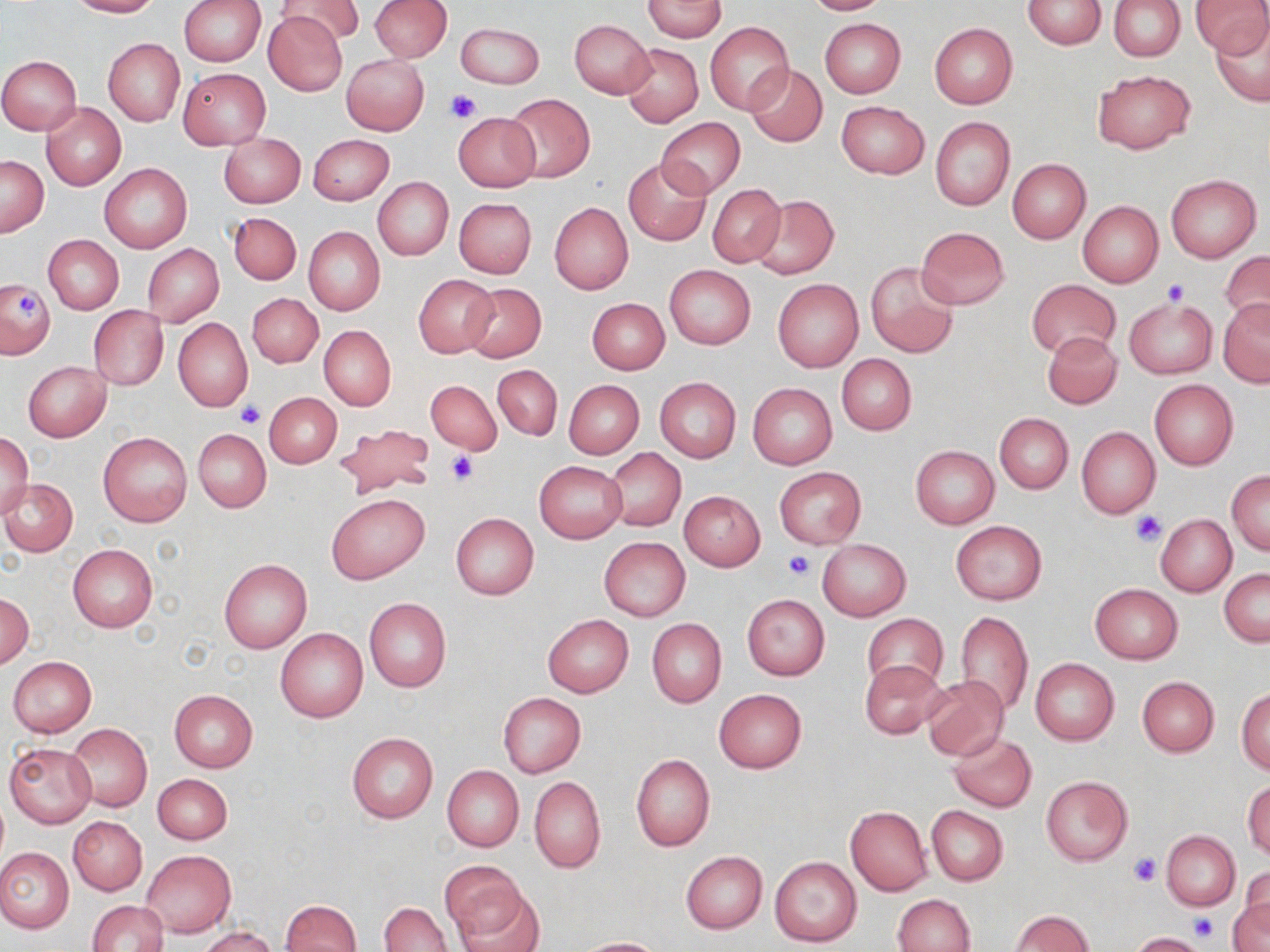

slide_level_diagnosis: negative for blood parasites
magnification: 1000x
stain: May-Grünwald-Giemsa
field_of_view: single
platelet_locations: 'approximate bounding boxes as (x1,y1)-(x2,y2) corner pairs in pixels: (445,89)-(480,123), (1162,279)-(1191,305), (16,291)-(44,315), (237,401)-(265,429), (444,450)-(478,485), (1131,510)-(1167,545), (783,551)-(813,581), (1128,851)-(1160,886), (1188,913)-(1220,943)'
modality: light microscopy
preparation: thin blood film
image_size: 1270×952 pixels
uninfected_red_blood_cell_locations: 'approximate bounding boxes as (x1,y1)-(x2,y2) corner pairs in pixels: (68,0)-(160,17), (178,0)-(264,66), (277,0)-(365,45), (370,0)-(451,62), (642,0)-(727,40), (802,0)-(890,15), (1022,0)-(1107,48), (1109,0)-(1185,61), (1192,1)-(1269,55), (262,10)-(348,97), (1209,15)-(1270,107), (819,18)-(906,98), (569,19)-(654,98), (826,19)-(910,179), (455,22)-(545,89), (705,22)-(793,114), (929,23)-(1017,107), (103,38)-(184,126), (620,43)-(703,128), (342,54)-(428,135), (0,56)-(81,135), (745,63)-(828,147), (179,69)-(269,149), (1092,70)-(1195,154), (504,93)-(595,183), (836,101)-(929,179), (41,103)-(125,190), (452,112)-(541,192), (929,116)-(1014,211), (657,119)-(746,197), (218,133)-(305,208), (308,134)-(393,205), (1,156)-(47,236), (623,158)-(712,247), (1007,159)-(1091,243), (100,163)-(191,252), (1165,174)-(1261,262), (372,178)-(453,261), (707,183)-(786,267), (749,195)-(838,280), (454,197)-(537,279), (1077,200)-(1163,286), (549,202)-(633,295), (228,213)-(301,284), (304,227)-(385,317), (916,227)-(1010,309), (44,235)-(123,314), (142,245)-(224,326), (1219,249)-(1270,330), (865,261)-(960,358), (664,265)-(755,349), (413,275)-(499,357), (0,278)-(55,359), (773,279)-(863,371), (1026,279)-(1121,358), (462,282)-(546,361), (247,294)-(323,368), (587,298)-(669,375), (1124,298)-(1217,379), (1218,298)-(1270,388), (90,306)-(168,390), (173,318)-(253,413), (319,325)-(395,410), (1042,332)-(1121,409), (837,354)-(917,436), (23,361)-(110,441), (493,365)-(563,440), (655,377)-(741,463), (565,379)-(645,459), (427,380)-(502,455), (1149,380)-(1238,469), (748,383)-(837,469), (264,392)-(342,468), (994,412)-(1074,493), (333,423)-(436,498), (1076,427)-(1160,518), (193,429)-(271,513), (99,432)-(192,526), (0,433)-(33,518), (910,445)-(999,529), (604,448)-(686,533), (534,461)-(625,543), (773,466)-(867,548), (1227,469)-(1270,555), (1,477)-(78,556), (679,491)-(765,571), (326,494)-(428,583), (451,513)-(539,600), (1157,516)-(1238,597), (950,521)-(1046,606), (598,537)-(690,620), (816,539)-(911,620), (68,544)-(157,632), (219,559)-(312,652), (1219,568)-(1269,647), (1089,583)-(1184,664), (0,593)-(33,668), (741,594)-(830,681), (364,597)-(451,691), (954,610)-(1033,716), (862,613)-(947,692), (542,614)-(633,697), (647,619)-(727,707), (275,627)-(368,723), (8,657)-(97,737), (860,659)-(947,738), (1031,659)-(1119,745), (921,675)-(1010,761), (1138,676)-(1219,757), (1237,687)-(1270,775), (169,689)-(258,773), (714,689)-(807,772), (498,692)-(585,778), (66,722)-(151,812), (347,732)-(438,824), (948,732)-(1037,812), (4,742)-(96,828), (630,754)-(715,851), (442,765)-(523,852), (153,773)-(232,844), (529,776)-(606,873), (1041,776)-(1133,865), (1244,779)-(1270,859), (926,806)-(1008,886), (845,807)-(932,896), (69,817)-(146,895), (1163,831)-(1240,911), (0,848)-(73,932), (141,849)-(235,937), (681,851)-(767,933), (769,856)-(863,947), (440,860)-(528,941), (1238,866)-(1268,939), (457,890)-(546,952), (891,894)-(975,952), (1229,897)-(1270,952), (280,899)-(362,952), (87,900)-(170,952), (379,901)-(451,952), (1009,910)-(1093,951), (200,927)-(278,952), (1130,931)-(1205,952), (576,937)-(668,952)'